State which parasite is depicted.
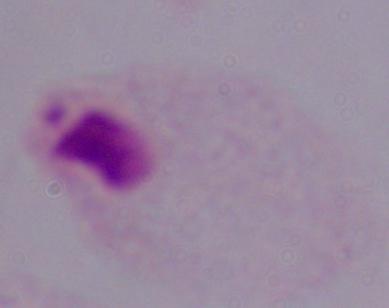
This is a trichomonad.

{
  "modality": "micrograph",
  "magnification": "1000x"
}